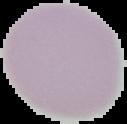
Summary:
  - Preparation: thin blood smear
  - Image type: cell region segmented out of the field of view; surrounding area masked to black
  - Result: negative for malaria parasites
  - Image size: 127×124 pixels